Comment on the morphology of the erythrocytes.
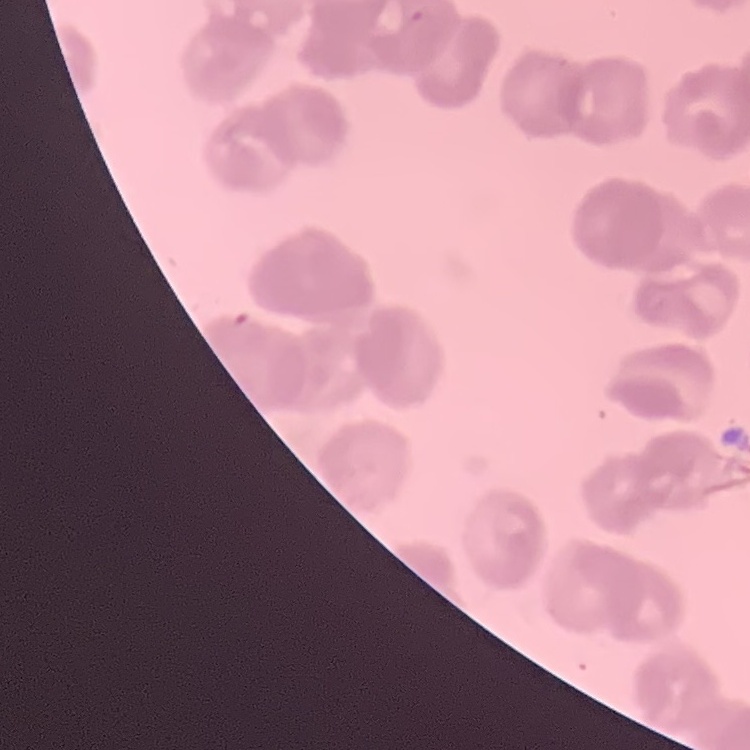

They show rouleaux formation.

Thin blood smear. Field's or Giemsa stain. Square crop of a larger photomicrograph.